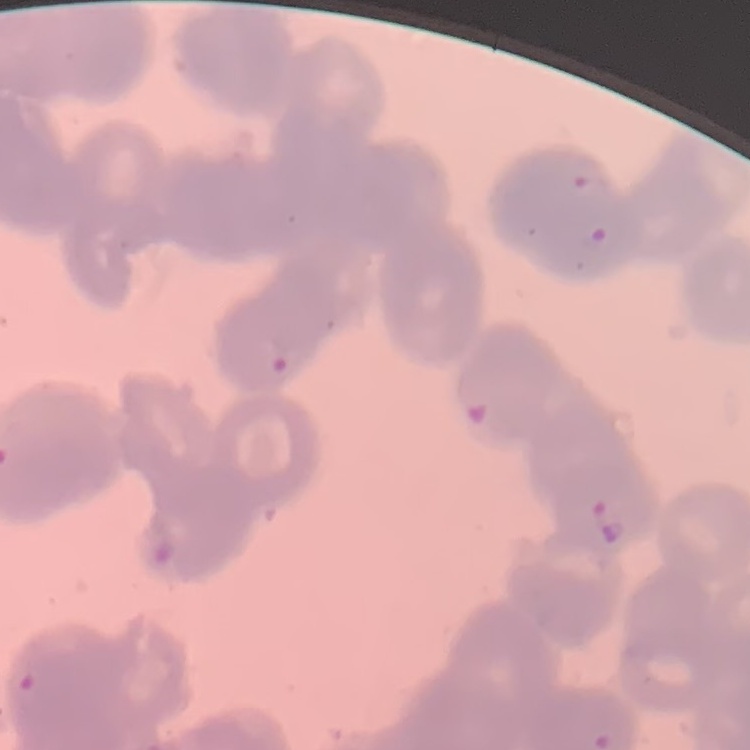
{
  "erythrocyte_morphology": "rouleaux formation",
  "preparation": "thin peripheral smear",
  "stain": "Field's or Giemsa",
  "image_type": "square crop of a larger photomicrograph"
}